Locate and identify every blood parasite.
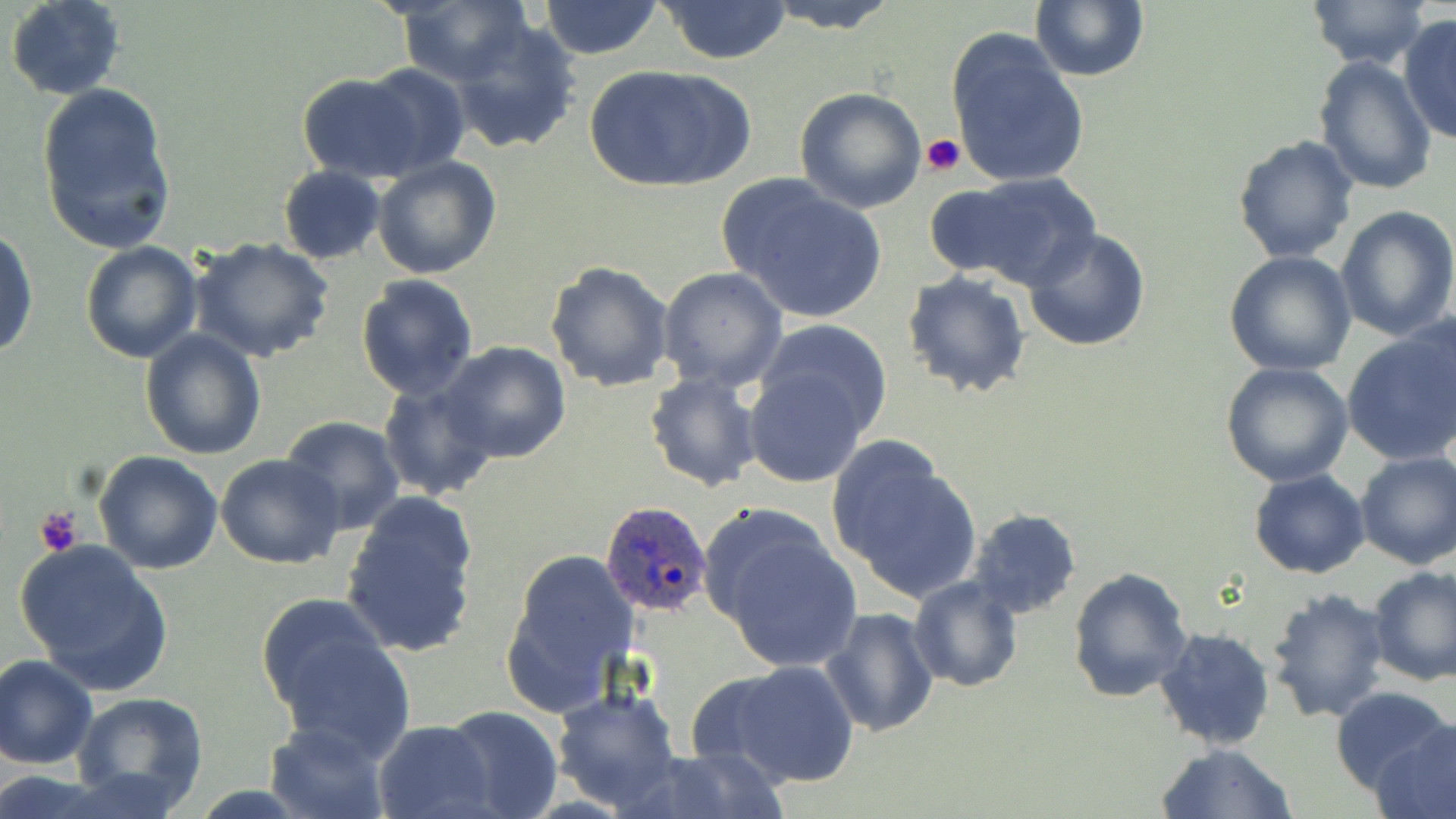

Approximate bounding boxes as (x1,y1)-(x2,y2) corner pairs in pixels.
Plasmodium ovale-infected red blood cells: (599,501)-(714,616).
No Plasmodium falciparum, Plasmodium malariae, Plasmodium vivax, Babesia divergens, or Trypanosoma brucei observed.

Summary:
  - Uninfected red blood cell locations: (6,0)-(126,100), (536,0)-(665,59), (656,0)-(794,65), (755,0)-(904,33), (1029,0)-(1149,82), (1302,0)-(1433,71), (394,3)-(531,87), (1397,14)-(1456,145), (448,15)-(582,156), (945,28)-(1091,190), (1313,56)-(1438,195), (352,63)-(473,176), (585,63)-(751,195), (294,73)-(431,182), (35,81)-(178,254), (794,87)-(927,213), (1232,133)-(1361,264), (372,157)-(501,280), (278,165)-(386,264), (927,175)-(1097,290), (722,178)-(890,324), (1334,204)-(1456,342), (1022,227)-(1151,352), (0,228)-(38,360), (190,237)-(335,364), (79,241)-(204,364), (1225,250)-(1357,376), (544,260)-(674,393), (657,267)-(788,392), (901,270)-(1032,399), (356,275)-(479,399), (1399,307)-(1456,448), (755,319)-(892,436), (1340,326)-(1456,468), (140,329)-(268,460), (437,342)-(572,464), (1222,361)-(1353,486), (742,362)-(875,490), (644,371)-(764,492), (377,378)-(497,501), (280,416)-(406,535), (826,437)-(982,606), (93,451)-(223,574), (1354,452)-(1456,570), (216,455)-(344,569), (1248,469)-(1371,579), (339,491)-(482,657), (968,509)-(1082,621), (700,510)-(863,674), (15,540)-(175,696), (500,546)-(639,717), (1367,565)-(1456,685), (1068,567)-(1194,704), (908,577)-(1024,693), (1265,586)-(1392,724), (257,594)-(412,757), (820,608)-(940,738), (1153,627)-(1275,751), (0,653)-(100,768), (707,659)-(861,788), (551,686)-(681,812), (1330,686)-(1456,800), (69,691)-(209,813), (440,706)-(563,819), (264,719)-(390,819), (372,720)-(495,819), (1373,722)-(1456,817), (1155,742)-(1297,819), (627,746)-(790,819)
  - Platelet locations: (921,133)-(965,176), (35,506)-(83,557)
  - Slide-level diagnosis: Plasmodium ovale
  - Field of view: one of a larger specimen
  - Preparation: thin blood film
  - Modality: light microscopy
  - Magnification: 1000x
  - Stain: May-Grünwald-Giemsa
  - Image size: 1456×819 pixels